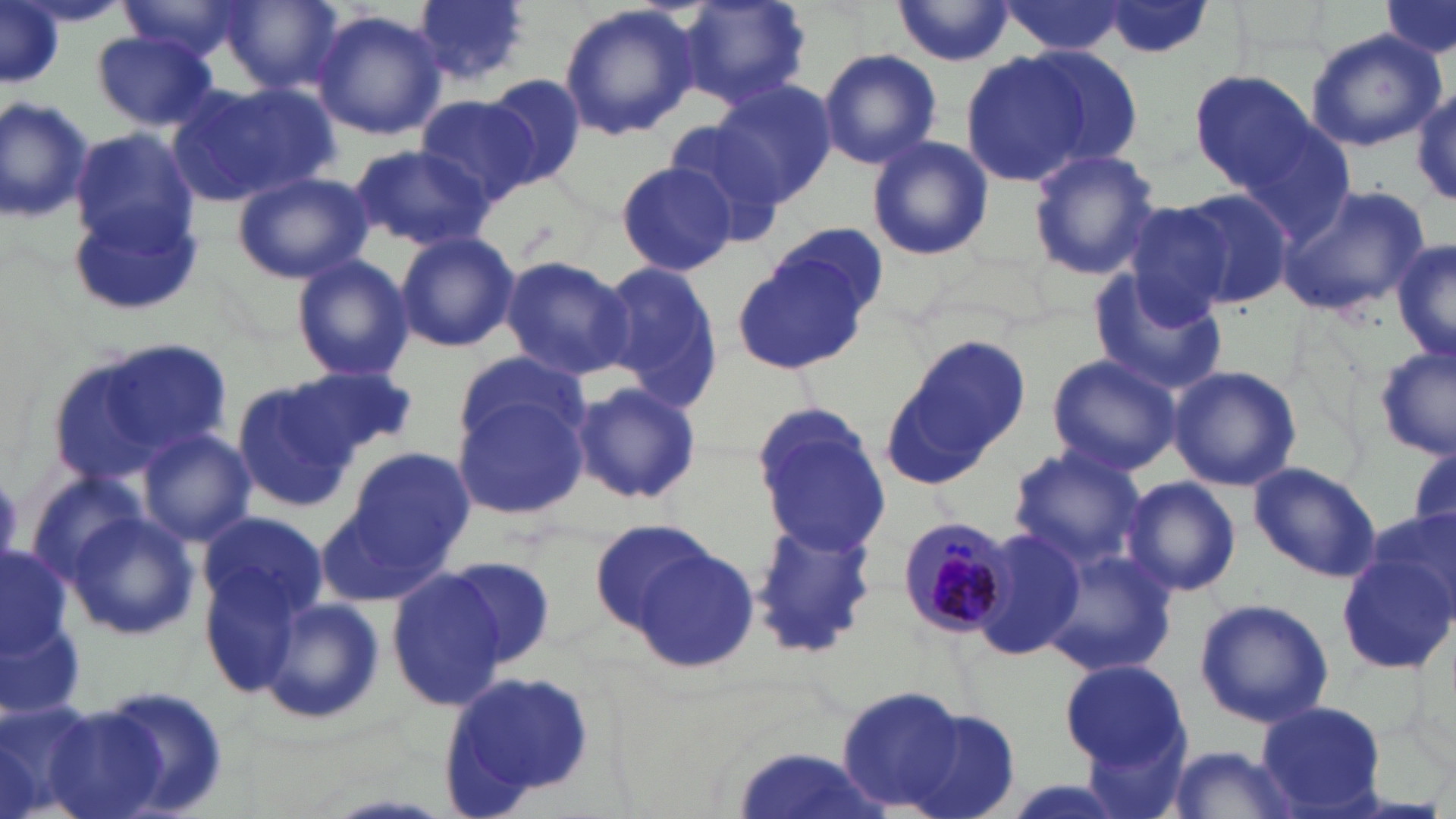

slide-level diagnosis = Plasmodium malariae
modality = light microscopy
field of view = one of a larger specimen
stain = May-Grünwald-Giemsa
preparation = thin blood smear
Plasmodium malariae-infected red blood cell locations = approximate bounding boxes as [x1, y1, x2, y2] in pixels: [898, 515, 1015, 642]
uninfected red blood cell locations = approximate bounding boxes as [x1, y1, x2, y2] in pixels: [0, 0, 60, 87], [115, 0, 255, 63], [411, 0, 533, 87], [679, 0, 811, 111], [1380, 0, 1454, 59], [217, 1, 345, 94], [992, 1, 1136, 57], [1093, 1, 1219, 62], [890, 3, 1022, 67], [558, 4, 701, 141], [312, 10, 447, 140], [1305, 29, 1443, 152], [90, 32, 219, 131], [1018, 46, 1143, 169], [818, 48, 941, 169], [959, 48, 1111, 186], [1189, 70, 1319, 185], [483, 75, 586, 188], [713, 79, 837, 205], [166, 80, 330, 209], [1410, 85, 1456, 209], [416, 92, 545, 208], [0, 94, 93, 227], [660, 119, 791, 247], [71, 128, 199, 258], [866, 135, 993, 262], [349, 143, 494, 252], [1026, 148, 1161, 281], [614, 160, 740, 277], [231, 171, 371, 284], [1276, 185, 1429, 318], [1165, 188, 1293, 313], [71, 196, 207, 315], [746, 227, 887, 358], [393, 230, 520, 353], [1392, 241, 1455, 367], [290, 253, 414, 383], [499, 256, 635, 381], [595, 261, 726, 413], [1086, 268, 1228, 394], [893, 334, 1031, 470], [48, 340, 233, 488], [1375, 343, 1456, 460], [452, 350, 586, 451], [1045, 353, 1181, 477], [1167, 364, 1303, 491], [289, 365, 417, 461], [224, 380, 355, 510], [570, 381, 703, 507], [451, 393, 588, 518], [755, 406, 888, 554], [136, 427, 256, 547], [1407, 441, 1456, 544], [346, 444, 474, 567], [1007, 447, 1146, 570], [1248, 460, 1382, 580], [25, 470, 153, 583], [1123, 476, 1241, 598], [318, 491, 457, 607], [58, 508, 201, 644], [195, 508, 329, 643], [1366, 509, 1456, 613], [749, 514, 878, 659], [589, 517, 721, 633], [969, 527, 1089, 662], [627, 543, 761, 677], [209, 545, 353, 728], [1038, 545, 1179, 679], [0, 547, 73, 660], [1337, 551, 1456, 673], [446, 555, 555, 670], [386, 566, 510, 712], [255, 596, 387, 727], [1195, 597, 1333, 728], [0, 621, 85, 722], [1061, 658, 1191, 770], [86, 683, 232, 819], [834, 687, 967, 809], [0, 696, 103, 819], [1258, 701, 1388, 814], [34, 702, 170, 819], [887, 707, 1020, 819], [1083, 728, 1193, 819], [730, 745, 888, 819], [1162, 745, 1304, 819]
image size = 1456×819 pixels
platelet locations = approximate bounding boxes as [x1, y1, x2, y2] in pixels: [0, 472, 26, 567]
magnification = 1000x